Identify the parasite.
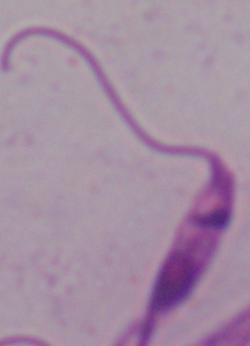
Leishmania.

{
  "modality": "micrograph",
  "magnification": "1000x"
}